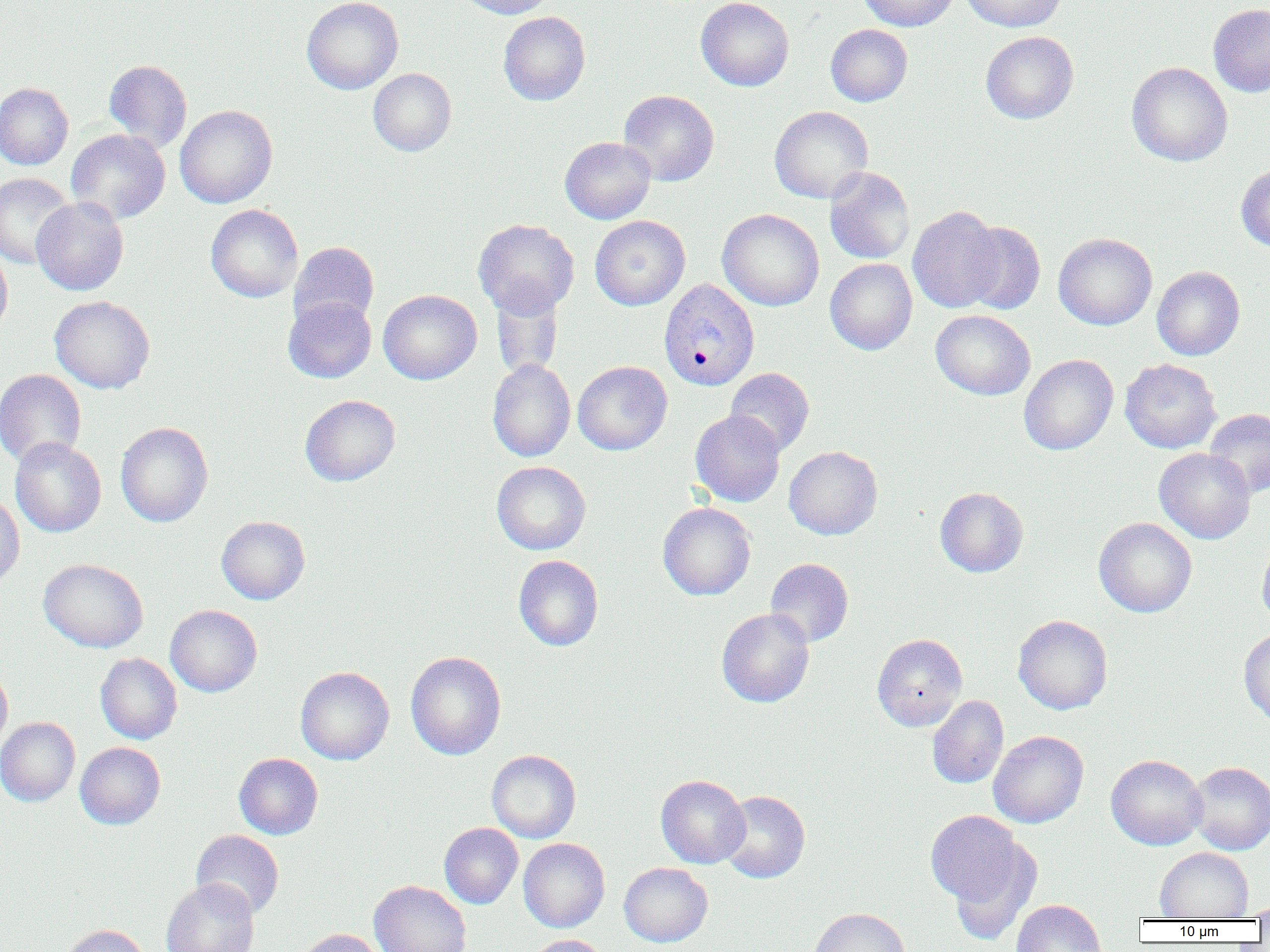

Summary:
  - Coordinate format: approximate bounding boxes as named x1/y1/x2/y2 corners in pixels
  - Plasmodium vivax-infected red blood cell locations: (x1=658, y1=279, x2=760, y2=392)
  - Uninfected red blood cell locations: (x1=301, y1=0, x2=403, y2=94), (x1=454, y1=0, x2=556, y2=19), (x1=696, y1=0, x2=794, y2=91), (x1=858, y1=0, x2=960, y2=31), (x1=960, y1=0, x2=1068, y2=32), (x1=1209, y1=4, x2=1270, y2=97), (x1=498, y1=11, x2=590, y2=106), (x1=826, y1=24, x2=912, y2=106), (x1=980, y1=31, x2=1079, y2=124), (x1=104, y1=59, x2=192, y2=152), (x1=1126, y1=62, x2=1232, y2=166), (x1=368, y1=68, x2=456, y2=156), (x1=0, y1=82, x2=73, y2=170), (x1=619, y1=89, x2=719, y2=186), (x1=174, y1=105, x2=277, y2=208), (x1=769, y1=105, x2=873, y2=204), (x1=66, y1=129, x2=171, y2=223), (x1=560, y1=136, x2=656, y2=224), (x1=1236, y1=164, x2=1270, y2=252), (x1=825, y1=167, x2=915, y2=264), (x1=0, y1=172, x2=74, y2=269), (x1=31, y1=197, x2=129, y2=295), (x1=205, y1=204, x2=304, y2=302), (x1=908, y1=206, x2=1006, y2=313), (x1=717, y1=208, x2=824, y2=311), (x1=590, y1=216, x2=690, y2=310), (x1=473, y1=218, x2=580, y2=317), (x1=959, y1=221, x2=1046, y2=315), (x1=1054, y1=232, x2=1157, y2=330), (x1=289, y1=242, x2=379, y2=329), (x1=0, y1=245, x2=12, y2=338), (x1=825, y1=258, x2=917, y2=355), (x1=1152, y1=266, x2=1245, y2=360), (x1=491, y1=284, x2=564, y2=381), (x1=378, y1=289, x2=482, y2=385), (x1=50, y1=295, x2=155, y2=394), (x1=283, y1=296, x2=377, y2=383), (x1=931, y1=309, x2=1035, y2=400), (x1=1019, y1=354, x2=1118, y2=456), (x1=487, y1=358, x2=576, y2=462), (x1=1120, y1=359, x2=1221, y2=453), (x1=573, y1=361, x2=672, y2=455), (x1=725, y1=368, x2=814, y2=457), (x1=0, y1=369, x2=86, y2=467), (x1=300, y1=394, x2=400, y2=486), (x1=1204, y1=408, x2=1270, y2=498), (x1=690, y1=409, x2=786, y2=507), (x1=115, y1=422, x2=213, y2=527), (x1=10, y1=437, x2=106, y2=537), (x1=784, y1=446, x2=883, y2=540), (x1=1154, y1=448, x2=1256, y2=543), (x1=491, y1=461, x2=591, y2=555), (x1=935, y1=487, x2=1028, y2=577), (x1=0, y1=493, x2=25, y2=589), (x1=658, y1=502, x2=756, y2=600), (x1=216, y1=516, x2=310, y2=604), (x1=1093, y1=517, x2=1197, y2=617), (x1=1257, y1=538, x2=1270, y2=628), (x1=513, y1=555, x2=603, y2=651), (x1=765, y1=558, x2=854, y2=647), (x1=39, y1=559, x2=148, y2=653), (x1=165, y1=604, x2=262, y2=697), (x1=717, y1=607, x2=815, y2=708), (x1=1013, y1=614, x2=1113, y2=714), (x1=1239, y1=628, x2=1270, y2=725), (x1=872, y1=633, x2=967, y2=731), (x1=405, y1=650, x2=506, y2=760), (x1=95, y1=653, x2=182, y2=744), (x1=0, y1=664, x2=12, y2=754), (x1=295, y1=666, x2=394, y2=765), (x1=927, y1=695, x2=1009, y2=789), (x1=0, y1=717, x2=80, y2=806), (x1=988, y1=730, x2=1089, y2=828), (x1=75, y1=742, x2=165, y2=829), (x1=486, y1=749, x2=581, y2=843), (x1=234, y1=753, x2=323, y2=839), (x1=1106, y1=754, x2=1207, y2=850), (x1=1186, y1=762, x2=1270, y2=855), (x1=656, y1=775, x2=750, y2=868), (x1=719, y1=790, x2=810, y2=883), (x1=925, y1=810, x2=1028, y2=911), (x1=439, y1=822, x2=523, y2=909), (x1=191, y1=829, x2=284, y2=919), (x1=518, y1=838, x2=610, y2=932), (x1=948, y1=844, x2=1041, y2=946), (x1=1155, y1=847, x2=1253, y2=920), (x1=619, y1=862, x2=712, y2=947), (x1=161, y1=878, x2=260, y2=952), (x1=369, y1=880, x2=471, y2=952), (x1=1011, y1=898, x2=1107, y2=952), (x1=1245, y1=900, x2=1270, y2=921), (x1=807, y1=907, x2=911, y2=952), (x1=59, y1=924, x2=151, y2=952), (x1=293, y1=928, x2=386, y2=952), (x1=525, y1=934, x2=611, y2=952)
  - Slide-level diagnosis: Plasmodium vivax
  - Modality: light microscopy
  - Preparation: thin blood smear
  - Field of view: single
  - Magnification: 1000x
  - Image size: 1270×952 pixels